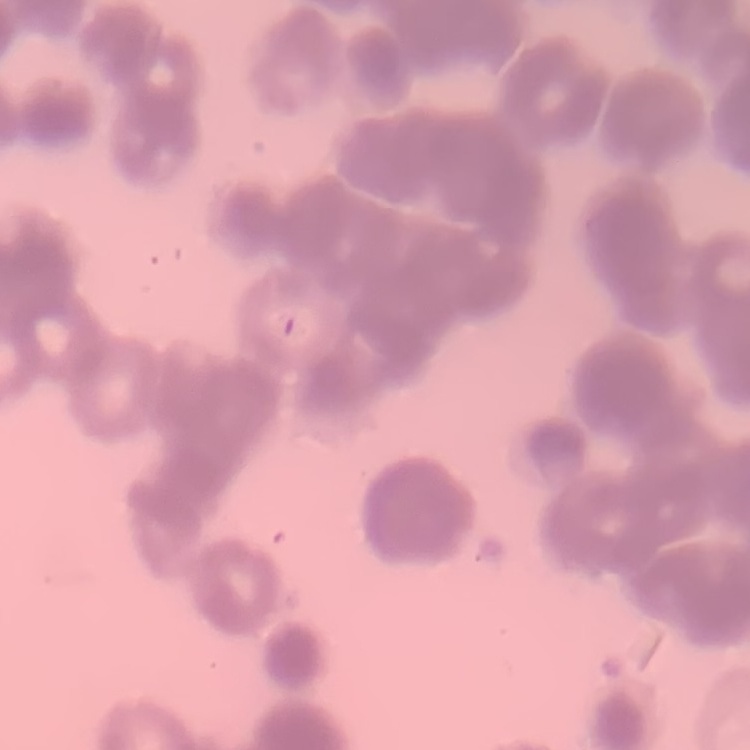

Summary:
  - Erythrocyte morphology: rouleaux formation
  - Image type: one tile cut from a larger photomicrograph
  - Preparation: thin blood film
  - Stain: Field's or Giemsa